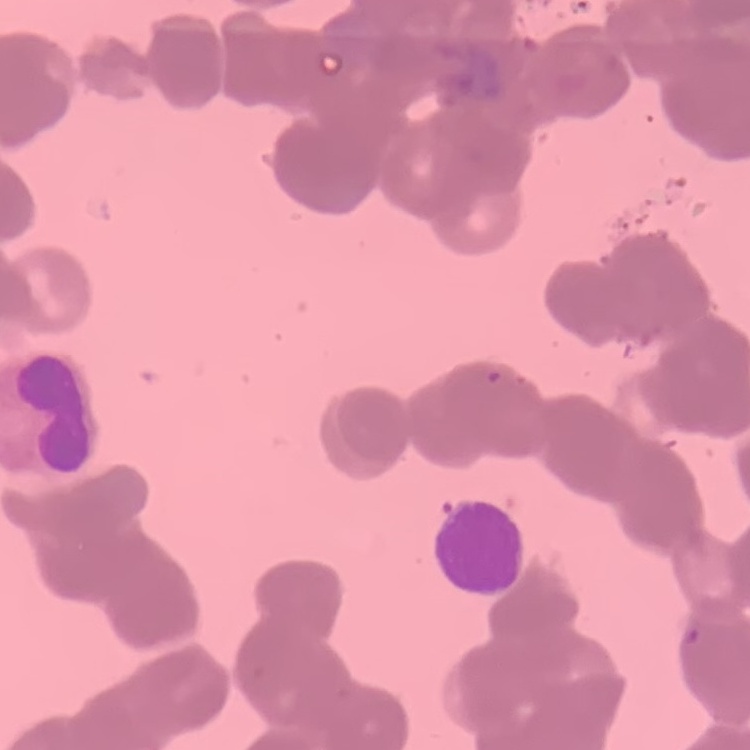 The erythrocytes show rouleaux formation. Thin blood film. Field's or Giemsa stain. One tile cut from a larger photomicrograph.